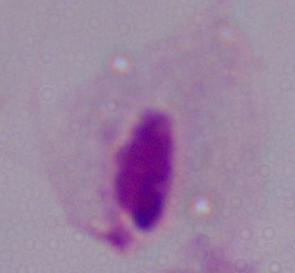
Summary:
  - Identification: trichomonad
  - Modality: micrograph
  - Magnification: 1000x